Find each parasitized red blood cell.
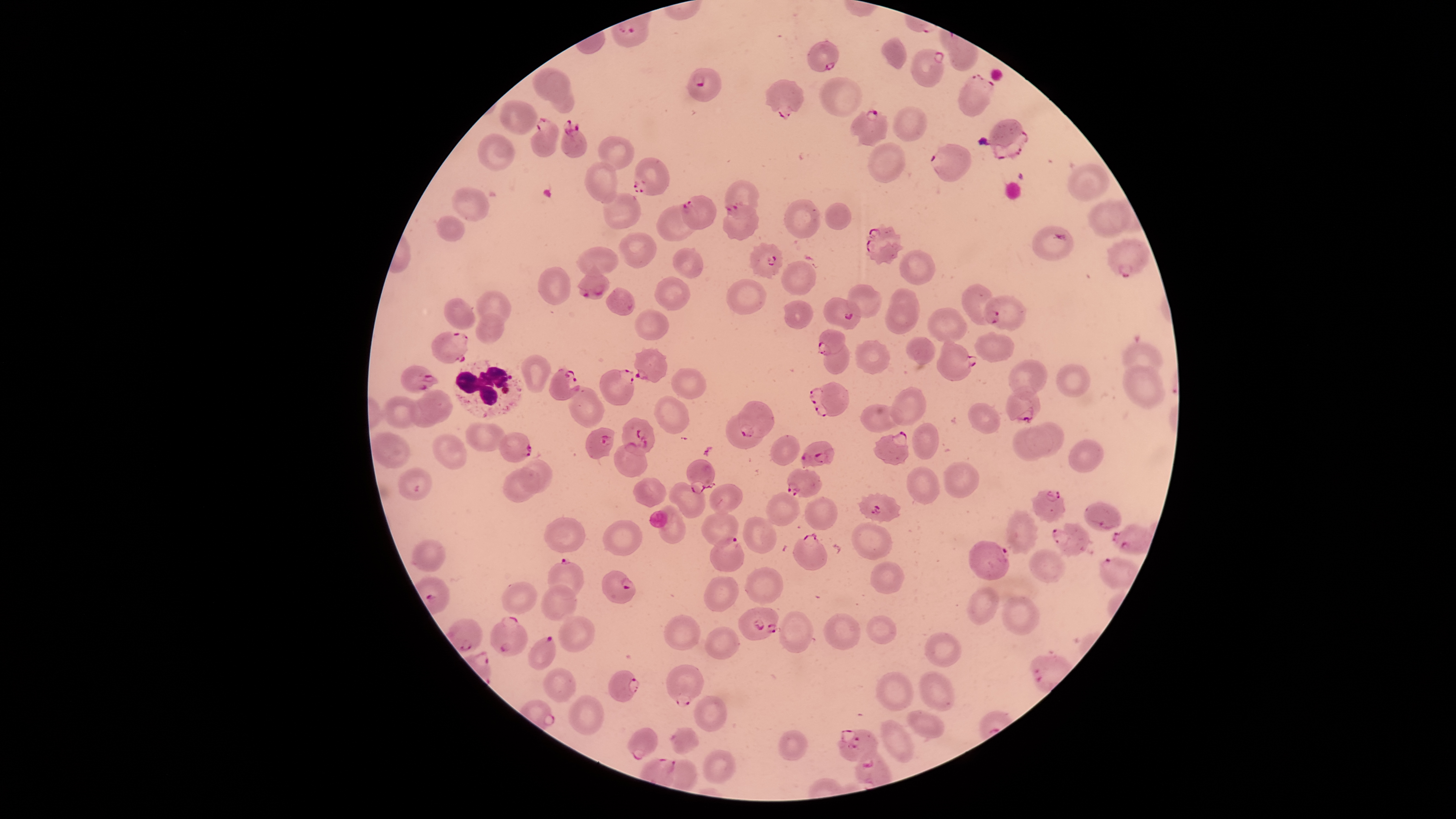
Approximate bounding boxes as {left, top, right, bottom} in pixels.
Parasitized red blood cells: {807, 41, 837, 72}, {911, 48, 944, 87}, {686, 68, 721, 103}, {957, 73, 995, 116}, {765, 79, 805, 119}, {849, 109, 889, 146}, {530, 117, 560, 157}, {561, 119, 587, 157}, {989, 119, 1028, 160}, {931, 143, 972, 183}, {633, 157, 668, 196}, {681, 193, 718, 230}, {722, 204, 758, 241}, {865, 222, 905, 265}, {1032, 225, 1074, 261}, {1106, 238, 1150, 278}, {749, 241, 782, 278}, {578, 262, 610, 300}, {984, 294, 1025, 331}, {822, 296, 861, 330}, {818, 329, 844, 355}, {431, 332, 468, 363}, {938, 338, 977, 381}, {633, 347, 667, 382}, {549, 364, 581, 400}, {400, 365, 440, 394}, {599, 368, 634, 406}, {809, 381, 848, 417}, {1005, 386, 1040, 424}, {738, 400, 775, 438}, {726, 412, 764, 448}, {622, 417, 655, 456}, {585, 428, 614, 459}, {874, 431, 909, 465}, {499, 432, 532, 462}, {799, 441, 836, 468}, {614, 442, 647, 477}, {686, 459, 715, 494}, {786, 468, 821, 497}, {1031, 490, 1066, 523}, {857, 492, 900, 523}, {1084, 502, 1121, 530}, {1053, 523, 1089, 556}, {1111, 525, 1150, 554}, {791, 531, 828, 570}, {709, 538, 744, 572}, {969, 540, 1009, 580}, {547, 557, 583, 598}, {1098, 557, 1139, 589}, {601, 570, 634, 604}, {738, 606, 779, 641}, {490, 616, 527, 656}, {446, 619, 482, 651}, {527, 635, 556, 668}, {667, 665, 704, 707}, {609, 670, 640, 701}, {627, 728, 658, 760}, {838, 730, 878, 763}, {855, 750, 892, 787}.

Approximate bounding boxes as {left, top, right, bottom} in pixels.
Summary:
  - White blood cells: {453, 360, 524, 419}
  - Uninfected red blood cells: {879, 37, 905, 70}, {532, 69, 571, 101}, {545, 71, 574, 112}, {819, 77, 862, 117}, {500, 99, 538, 134}, {892, 105, 927, 141}, {478, 134, 515, 170}, {598, 136, 635, 170}, {869, 143, 907, 182}, {584, 161, 617, 204}, {1068, 163, 1110, 201}, {724, 179, 760, 219}, {452, 187, 489, 221}, {603, 193, 641, 230}, {784, 198, 819, 238}, {1088, 201, 1131, 238}, {824, 202, 851, 230}, {656, 204, 700, 240}, {436, 215, 465, 241}, {618, 231, 657, 269}, {577, 246, 618, 277}, {673, 247, 704, 277}, {899, 250, 936, 284}, {781, 261, 816, 295}, {538, 268, 570, 305}, {654, 276, 691, 311}, {726, 278, 768, 315}, {846, 283, 883, 317}, {961, 284, 996, 325}, {605, 287, 636, 315}, {888, 288, 919, 326}, {477, 290, 510, 326}, {444, 297, 476, 329}, {784, 300, 812, 329}, {885, 302, 918, 333}, {928, 308, 969, 344}, {635, 309, 669, 340}, {475, 312, 503, 344}, {974, 333, 1014, 362}, {905, 337, 936, 364}, {823, 338, 849, 375}, {854, 340, 889, 375}, {1122, 342, 1162, 377}, {521, 353, 550, 391}, {1007, 359, 1047, 401}, {1056, 364, 1090, 397}, {1123, 366, 1165, 408}, {671, 367, 706, 398}, {568, 386, 605, 428}, {889, 386, 927, 426}, {419, 389, 452, 423}, {382, 396, 419, 429}, {654, 397, 690, 433}, {408, 398, 442, 427}, {968, 402, 1000, 435}, {912, 422, 938, 459}, {1025, 422, 1066, 456}, {466, 423, 508, 451}, {1013, 427, 1053, 462}, {375, 434, 411, 467}, {433, 434, 466, 469}, {770, 435, 799, 465}, {1067, 439, 1104, 472}, {518, 458, 552, 494}, {944, 463, 980, 499}, {907, 466, 939, 505}, {398, 468, 433, 500}, {503, 468, 541, 502}, {633, 477, 667, 509}, {669, 481, 705, 519}, {709, 484, 744, 515}, {765, 491, 799, 526}, {805, 497, 837, 529}, {657, 506, 685, 544}, {1006, 508, 1038, 555}, {700, 511, 738, 547}, {543, 517, 586, 553}, {742, 517, 777, 553}, {601, 518, 641, 555}, {852, 522, 892, 559}, {412, 540, 446, 571}, {1029, 549, 1066, 582}, {871, 561, 904, 594}, {745, 567, 782, 604}, {703, 576, 740, 612}, {500, 580, 537, 615}, {541, 584, 576, 621}, {966, 586, 998, 624}, {1001, 595, 1040, 635}, {777, 611, 813, 653}, {824, 613, 861, 650}, {665, 614, 700, 650}, {559, 615, 595, 653}, {866, 616, 897, 644}, {705, 626, 740, 659}, {924, 631, 961, 668}, {541, 668, 575, 701}, {876, 672, 913, 710}, {568, 695, 606, 735}, {694, 697, 727, 731}, {907, 710, 945, 737}, {879, 719, 914, 761}, {672, 728, 700, 756}, {778, 729, 806, 761}, {701, 750, 735, 783}, {661, 759, 698, 788}
  - Capture: smartphone photograph through the microscope eyepiece
  - Visible region: circular
  - Preparation: thin blood film
  - Stain: Giemsa
  - Field of view: single
  - Species: Plasmodium falciparum
  - Image size: 1456×819 pixels